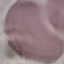 Malaria status: uninfected. Giemsa stain. Automatically extracted cell patch, resized to 64 × 64 pixels. Acquired by smartphone through the microscope eyepiece. Thin smear of blood.